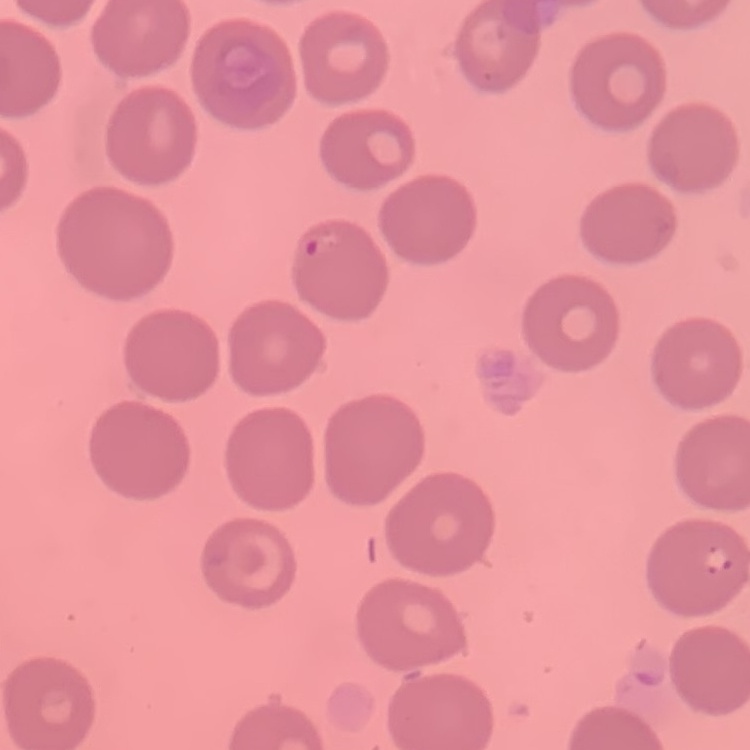

Summary:
  - Erythrocyte morphology: no rouleaux formation
  - Image type: one tile cut from a larger photomicrograph
  - Preparation: thin peripheral smear
  - Stain: Field's or Giemsa